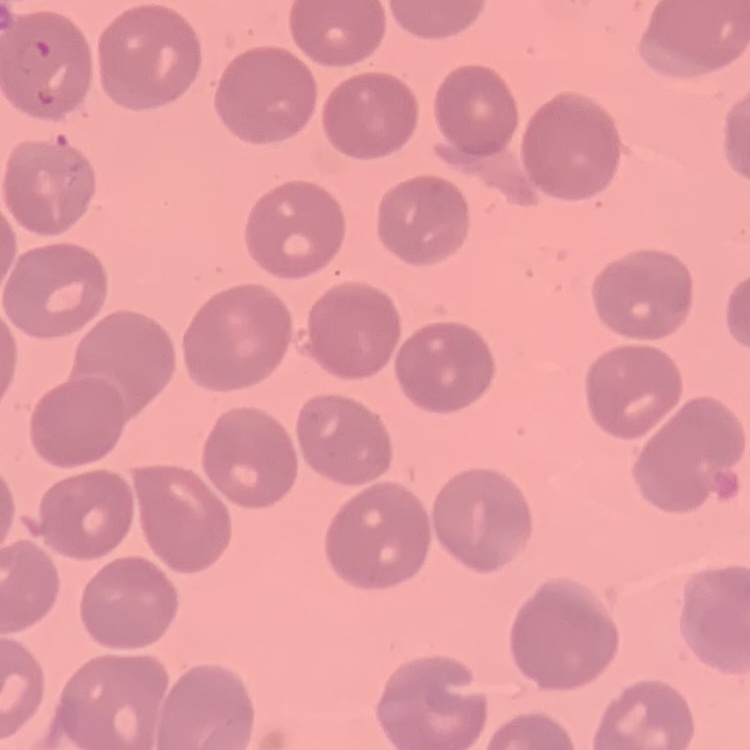

red blood cell morphology = no rouleaux formation
preparation = thin peripheral smear
stain = Field's or Giemsa
image type = one tile cut from a larger photomicrograph